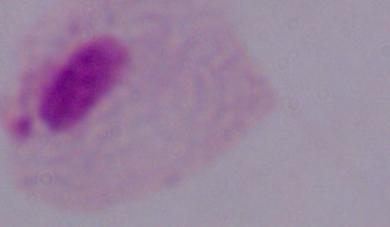
Summary:
  - Modality: micrograph
  - Magnification: 1000x
  - Identification: trichomonad